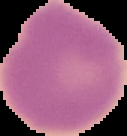

malaria status = uninfected
image size = 127×136 pixels
preparation = thin blood film
image type = segmented cell region on a black background